Outline every leukocyte.
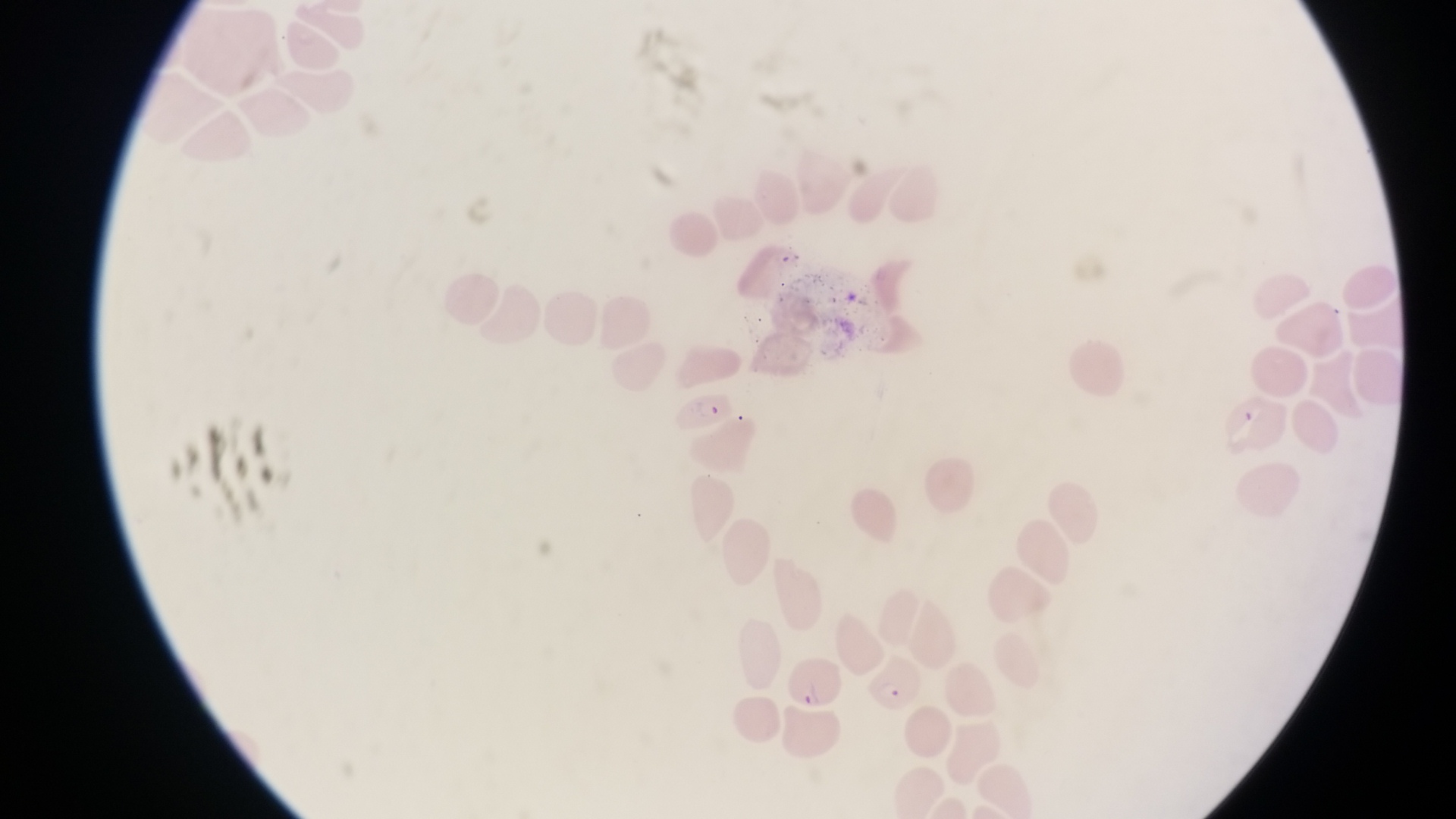
No leukocytes observed.

capture: smartphone photograph through the eyepiece of an Olympus CX-23 microscope
image_size: 1456×819 pixels
parasitised_red_blood_cell_locations: 'approximate bounding boxes as (left, top, right, bottom) in pixels: (670, 386, 733, 435), (785, 648, 841, 708), (869, 650, 924, 711)'
preparation: thin blood film
magnification: 1000x
country: Uganda
field_of_view: single
artifact_platelet_like_body_stain_precipitate_or_debris_locations: 'approximate bounding boxes as (left, top, right, bottom) in pixels: (1237, 397, 1266, 429)'